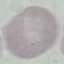
Summary:
  - Result: no malaria parasites seen
  - Image type: automatically extracted cell patch, resized to 64 × 64 pixels
  - Capture: smartphone through the microscope eyepiece
  - Stain: Giemsa
  - Preparation: thin blood smear